Locate and identify every blood parasite.
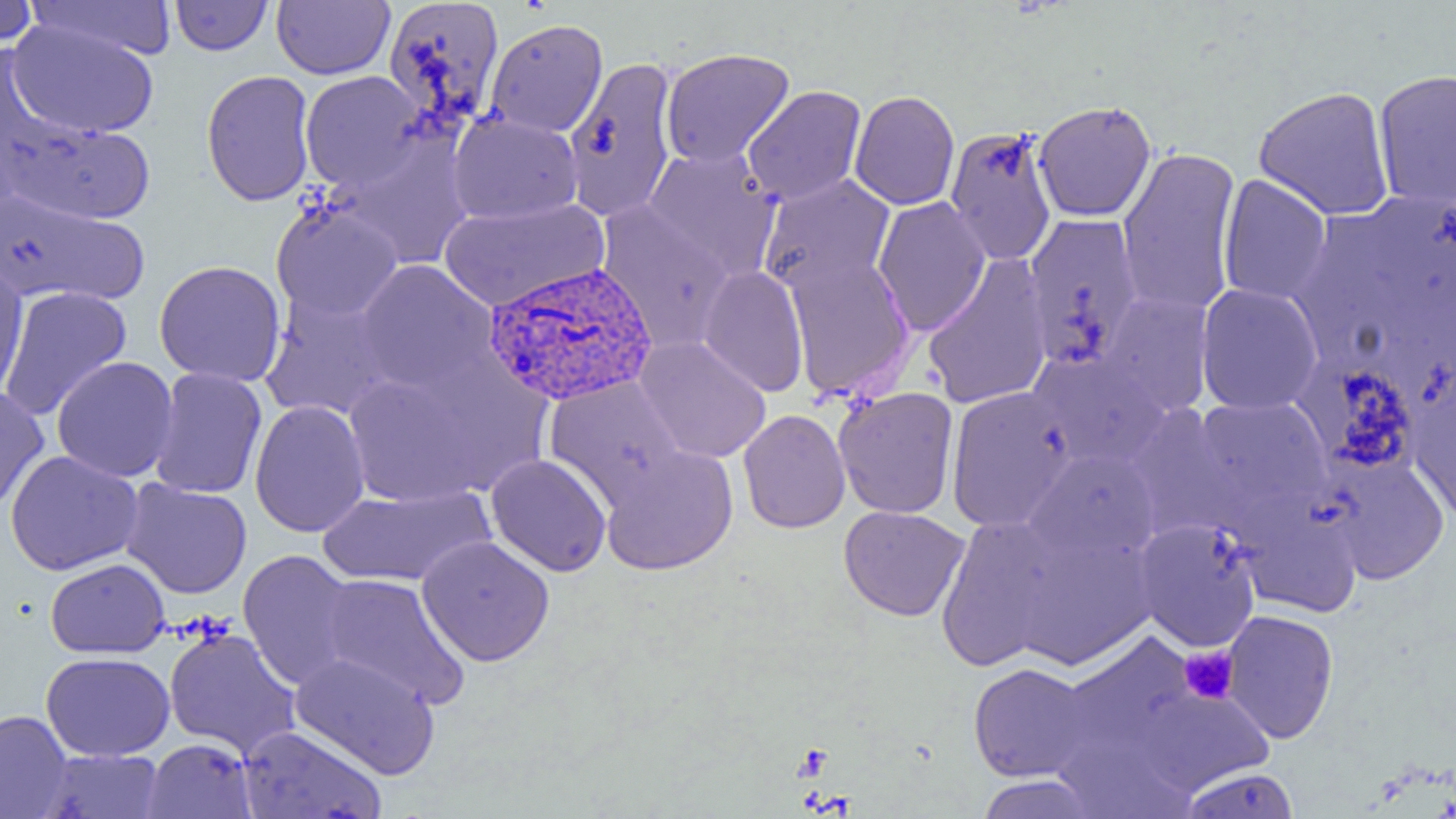

Approximate bounding boxes as named x1/y1/x2/y2 corners in pixels.
Plasmodium vivax-infected red blood cells: (x1=482, y1=261, x2=659, y2=406).
No Plasmodium falciparum, Plasmodium ovale, Plasmodium malariae, Babesia divergens, or Trypanosoma brucei observed.

Uninfected red blood cell locations: (x1=25, y1=0, x2=176, y2=62), (x1=170, y1=0, x2=272, y2=56), (x1=272, y1=0, x2=394, y2=80), (x1=0, y1=1, x2=40, y2=49), (x1=382, y1=1, x2=505, y2=135), (x1=484, y1=18, x2=608, y2=138), (x1=8, y1=19, x2=159, y2=138), (x1=660, y1=48, x2=795, y2=169), (x1=562, y1=57, x2=680, y2=222), (x1=1373, y1=68, x2=1456, y2=209), (x1=201, y1=70, x2=316, y2=207), (x1=299, y1=70, x2=427, y2=192), (x1=742, y1=85, x2=866, y2=206), (x1=1253, y1=85, x2=1395, y2=221), (x1=849, y1=90, x2=960, y2=210), (x1=1033, y1=100, x2=1156, y2=222), (x1=447, y1=111, x2=583, y2=225), (x1=3, y1=112, x2=156, y2=226), (x1=944, y1=125, x2=1058, y2=266), (x1=336, y1=137, x2=475, y2=270), (x1=642, y1=146, x2=781, y2=282), (x1=1116, y1=146, x2=1242, y2=317), (x1=758, y1=174, x2=895, y2=295), (x1=1218, y1=174, x2=1332, y2=306), (x1=0, y1=188, x2=151, y2=307), (x1=1363, y1=193, x2=1456, y2=322), (x1=438, y1=196, x2=608, y2=312), (x1=872, y1=197, x2=992, y2=335), (x1=270, y1=199, x2=404, y2=323), (x1=596, y1=203, x2=734, y2=351), (x1=1289, y1=211, x2=1406, y2=357), (x1=1022, y1=214, x2=1145, y2=370), (x1=783, y1=254, x2=915, y2=402), (x1=922, y1=254, x2=1053, y2=409), (x1=0, y1=255, x2=29, y2=402), (x1=154, y1=259, x2=287, y2=386), (x1=355, y1=260, x2=498, y2=395), (x1=698, y1=265, x2=810, y2=398), (x1=1195, y1=283, x2=1323, y2=416), (x1=0, y1=286, x2=133, y2=422), (x1=260, y1=291, x2=398, y2=423), (x1=1097, y1=291, x2=1216, y2=417), (x1=633, y1=337, x2=772, y2=463), (x1=1029, y1=352, x2=1171, y2=470), (x1=51, y1=356, x2=179, y2=483), (x1=340, y1=357, x2=531, y2=509), (x1=1305, y1=359, x2=1425, y2=479), (x1=149, y1=367, x2=268, y2=499), (x1=1407, y1=370, x2=1456, y2=525), (x1=543, y1=376, x2=688, y2=506), (x1=0, y1=386, x2=49, y2=515), (x1=945, y1=386, x2=1077, y2=531), (x1=833, y1=387, x2=959, y2=519), (x1=1192, y1=396, x2=1332, y2=516), (x1=249, y1=400, x2=370, y2=537), (x1=1127, y1=405, x2=1248, y2=541), (x1=737, y1=409, x2=850, y2=533), (x1=600, y1=445, x2=738, y2=575), (x1=1024, y1=448, x2=1161, y2=564), (x1=4, y1=450, x2=144, y2=575), (x1=486, y1=454, x2=612, y2=577), (x1=1322, y1=456, x2=1450, y2=583), (x1=120, y1=479, x2=252, y2=599), (x1=316, y1=484, x2=494, y2=588), (x1=1235, y1=496, x2=1363, y2=618), (x1=838, y1=505, x2=970, y2=621), (x1=936, y1=515, x2=1061, y2=671), (x1=1134, y1=518, x2=1262, y2=652), (x1=1015, y1=533, x2=1156, y2=670), (x1=416, y1=535, x2=555, y2=667), (x1=238, y1=549, x2=360, y2=691), (x1=45, y1=558, x2=170, y2=658), (x1=318, y1=573, x2=470, y2=709), (x1=1221, y1=609, x2=1339, y2=744), (x1=164, y1=627, x2=302, y2=760), (x1=1059, y1=633, x2=1198, y2=765), (x1=41, y1=651, x2=175, y2=761), (x1=289, y1=652, x2=441, y2=780), (x1=967, y1=662, x2=1094, y2=782), (x1=1127, y1=684, x2=1274, y2=796), (x1=0, y1=710, x2=72, y2=819), (x1=238, y1=725, x2=387, y2=819), (x1=1052, y1=728, x2=1199, y2=819), (x1=142, y1=738, x2=257, y2=818), (x1=36, y1=748, x2=165, y2=818), (x1=1179, y1=767, x2=1299, y2=818), (x1=975, y1=775, x2=1099, y2=818). Platelet locations: (x1=1179, y1=646, x2=1239, y2=704). Slide-level diagnosis: Plasmodium vivax. Image is 1456×819 pixels. Captured at 1000x magnification. One field of a larger specimen. Thin blood smear. Optical microscopy.